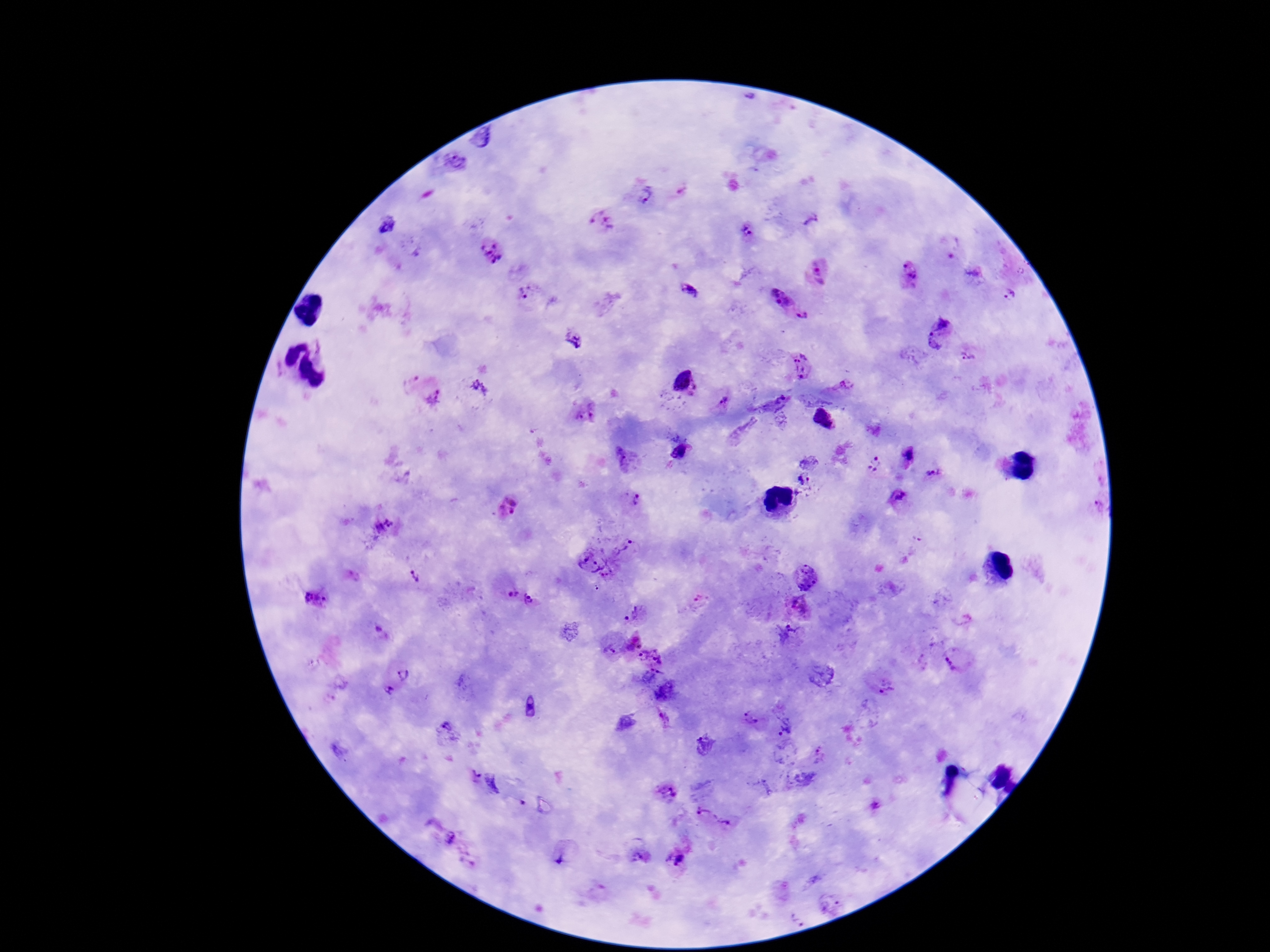
Approximate centers as (x, y) in pixels.
Summary:
  - Plasmodium parasite locations: (749, 97), (484, 139), (453, 161), (644, 194), (600, 220), (810, 220), (386, 224), (748, 233), (492, 253), (818, 273), (909, 275), (524, 291), (687, 291), (1011, 294), (781, 296), (804, 317), (938, 331), (575, 341), (969, 353), (800, 364), (685, 383), (844, 384), (480, 389), (435, 396), (773, 403), (724, 404), (584, 412), (823, 417), (783, 420), (683, 448), (907, 456), (625, 457), (808, 462), (874, 464), (932, 473), (804, 481), (898, 495), (632, 500), (509, 506), (383, 529), (623, 549), (587, 564), (610, 575), (412, 576), (808, 579), (515, 591), (315, 598), (700, 600), (536, 603), (799, 607), (631, 615), (786, 634), (632, 640), (608, 649), (651, 652), (954, 660), (403, 673), (652, 678), (886, 688), (389, 691), (532, 706), (751, 717), (664, 718), (786, 724), (448, 730), (706, 745), (820, 754), (475, 774), (803, 780), (495, 784), (664, 795), (875, 806), (707, 813), (725, 823), (453, 837), (562, 855), (643, 857), (676, 859), (830, 901)
  - Capture: smartphone camera through the microscope eyepiece
  - Field of view: one from this slide
  - Magnification: 100x
  - Image size: 1270×952 pixels
  - Stain: Giemsa
  - Patient malaria status: infected
  - Preparation: thick blood smear